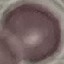 Malaria status: uninfected. Cell patch, automatically extracted from a larger field of view and resized to 64 × 64 pixels. Photographed with a smartphone camera at the microscope eyepiece. Thin blood smear. Giemsa-stained preparation.